Identify the parasite.
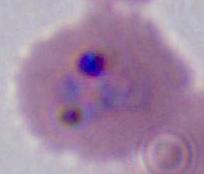

Plasmodium.

magnification = 400x or 1000x
modality = photomicrograph